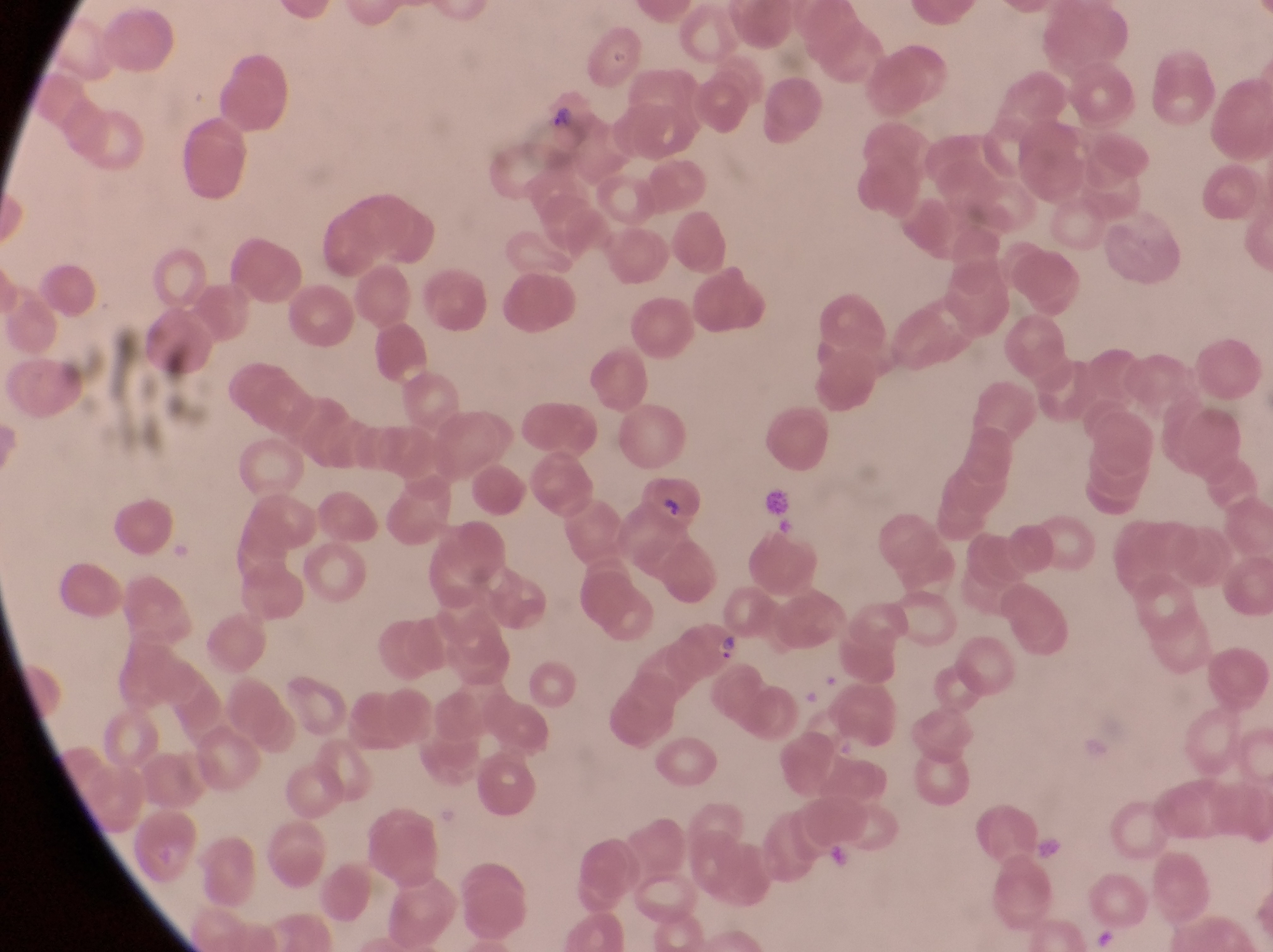

Approximate bounding boxes as left top right bottom in pixels.
Summary:
  - Artifact (platelet-like body, stain precipitate, or debris) locations: 756 482 793 529; 1031 829 1061 869
  - Parasitised red blood cell locations: 525 89 594 146; 639 467 704 532; 679 612 739 674
  - Preparation: thin blood film
  - Capture: smartphone photograph through the eyepiece of an Olympus CX-23 microscope
  - Country: Uganda
  - Magnification: 1000x
  - Image size: 1273×952 pixels
  - Field of view: single